Identify the parasite.
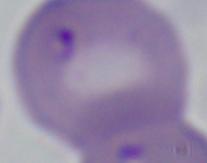
This is Babesia.

modality = photomicrograph
magnification = 1000x